Assess this cell for malaria.
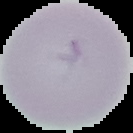
It is uninfected.

From a thin blood film. Image is 133×133 pixels. Cell region segmented out of the field of view; the surrounding area is masked to black.